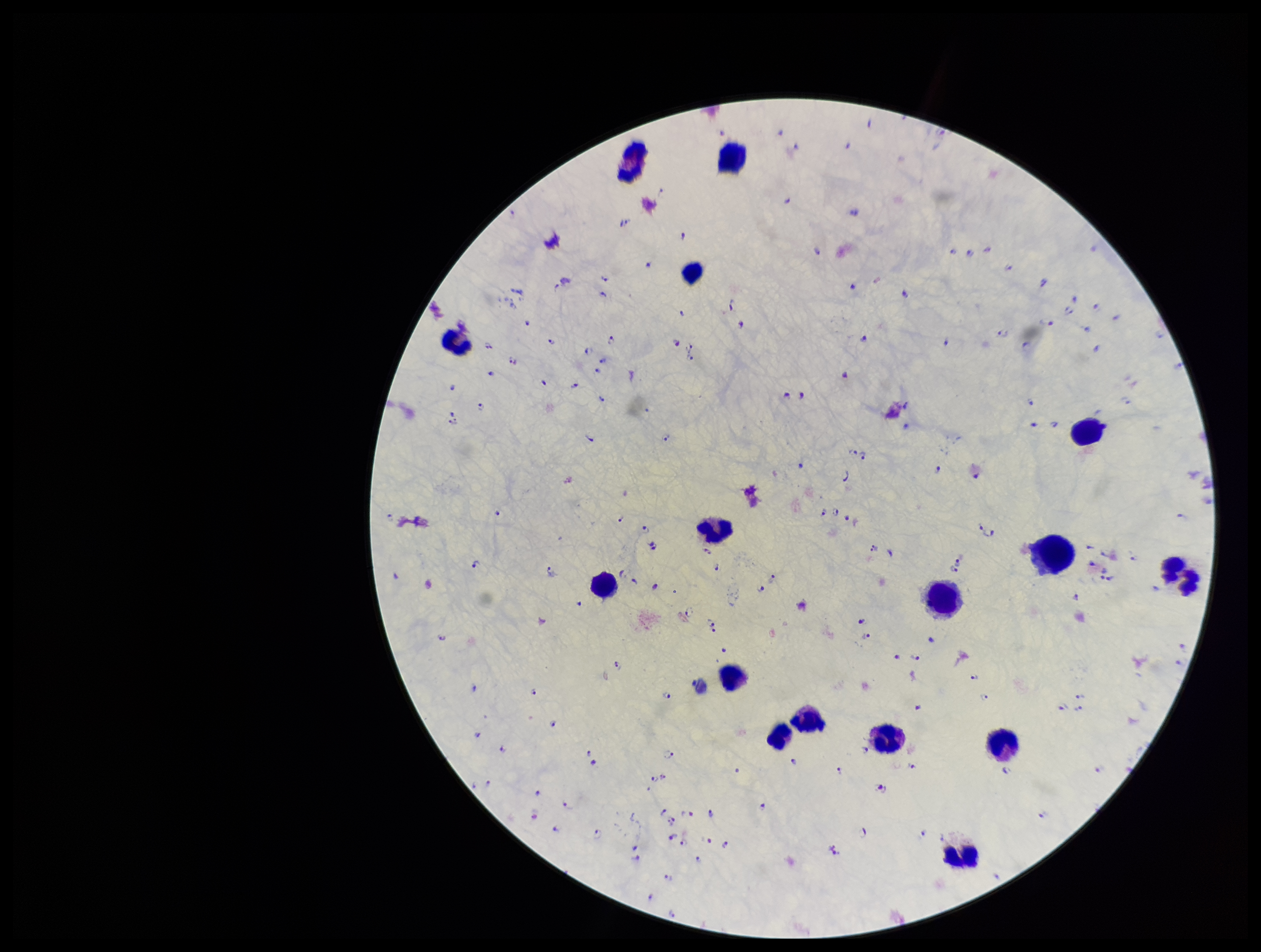
Leukocyte count: 15. One field from this slide. Species reported for this patient: Plasmodium falciparum. Photographed through the microscope eyepiece with a smartphone camera. Patient malaria status: infected. Image is 1261×952 pixels. Plasmodium parasites: seen. Stained with Giemsa. Parasite count: 185. Preparation: thick.